Outline each blood parasite and name the species.
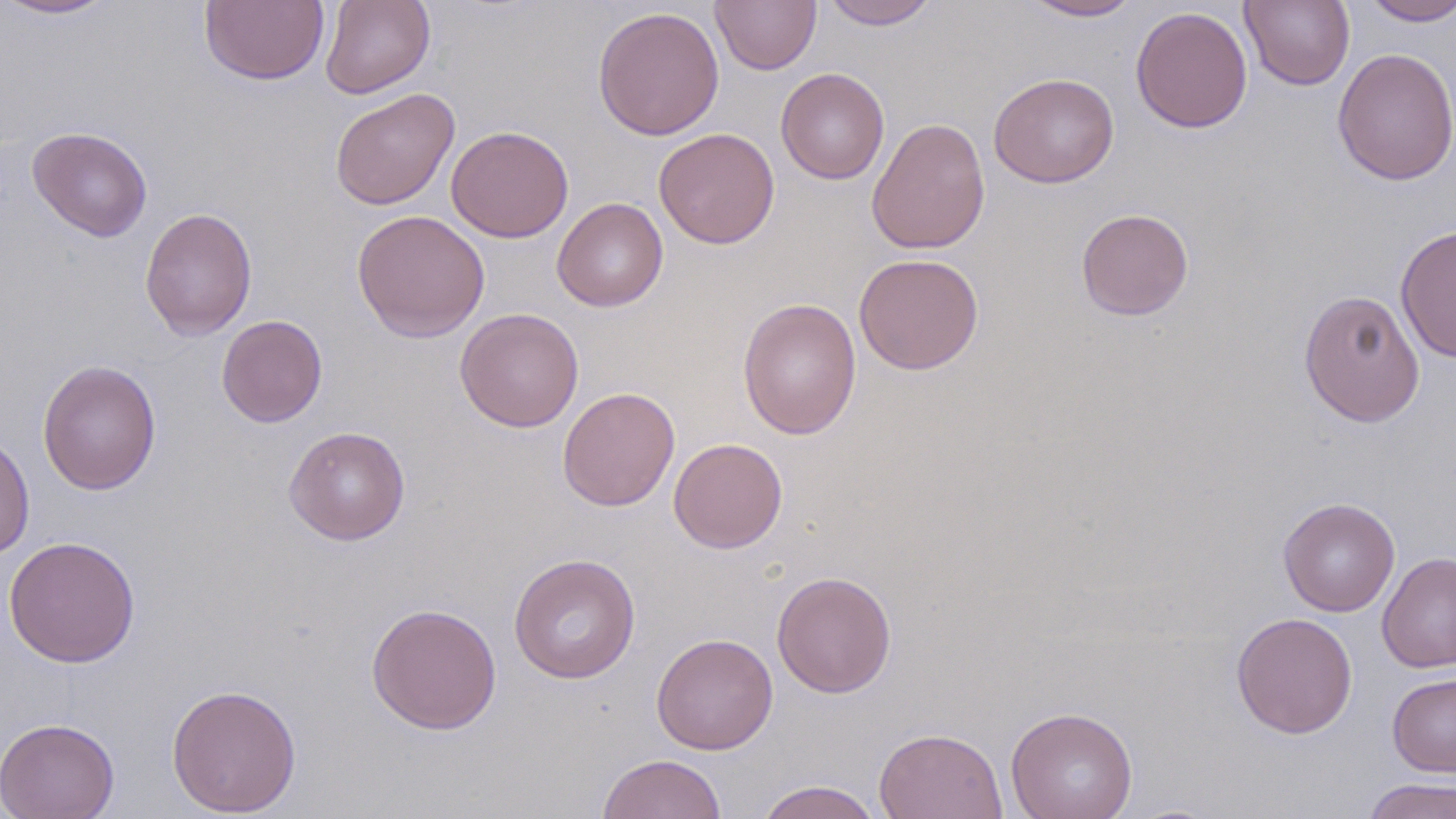

No blood parasites observed.

Summary:
  - Coordinate format: approximate bounding boxes as [x1, y1, x2, y2] in pixels
  - Uninfected red blood cell locations: [1, 0, 118, 20], [199, 0, 329, 85], [319, 0, 436, 99], [821, 0, 940, 29], [1239, 0, 1355, 91], [710, 1, 821, 74], [1020, 1, 1142, 21], [1359, 1, 1456, 26], [592, 6, 725, 141], [1130, 6, 1253, 134], [1332, 47, 1456, 186], [776, 67, 889, 185], [989, 72, 1119, 188], [329, 88, 460, 210], [866, 118, 990, 254], [446, 125, 574, 243], [27, 126, 153, 242], [654, 128, 780, 249], [552, 197, 668, 311], [139, 207, 257, 341], [1076, 208, 1194, 321], [352, 209, 489, 343], [1395, 224, 1456, 363], [853, 253, 984, 375], [1298, 289, 1425, 427], [737, 297, 862, 440], [455, 308, 584, 432], [216, 314, 328, 427], [37, 359, 162, 496], [558, 386, 680, 511], [284, 426, 410, 545], [0, 430, 35, 561], [668, 437, 788, 553], [1277, 497, 1400, 616], [2, 535, 141, 668], [1377, 551, 1456, 674], [508, 553, 641, 683], [771, 570, 896, 698], [366, 602, 502, 734], [1230, 612, 1358, 739], [651, 632, 778, 754], [1387, 671, 1456, 777], [166, 683, 302, 817], [1006, 706, 1138, 819], [0, 716, 120, 819], [873, 727, 1008, 819], [597, 753, 727, 818], [1361, 777, 1456, 819], [755, 780, 884, 819]
  - Slide-level diagnosis: no evidence of blood parasites
  - Preparation: thin blood smear
  - Stain: May-Grünwald-Giemsa
  - Field of view: single
  - Magnification: 1000x
  - Image size: 1456×819 pixels
  - Modality: light microscopy